Locate every Plasmodium falciparum-infected red blood cell.
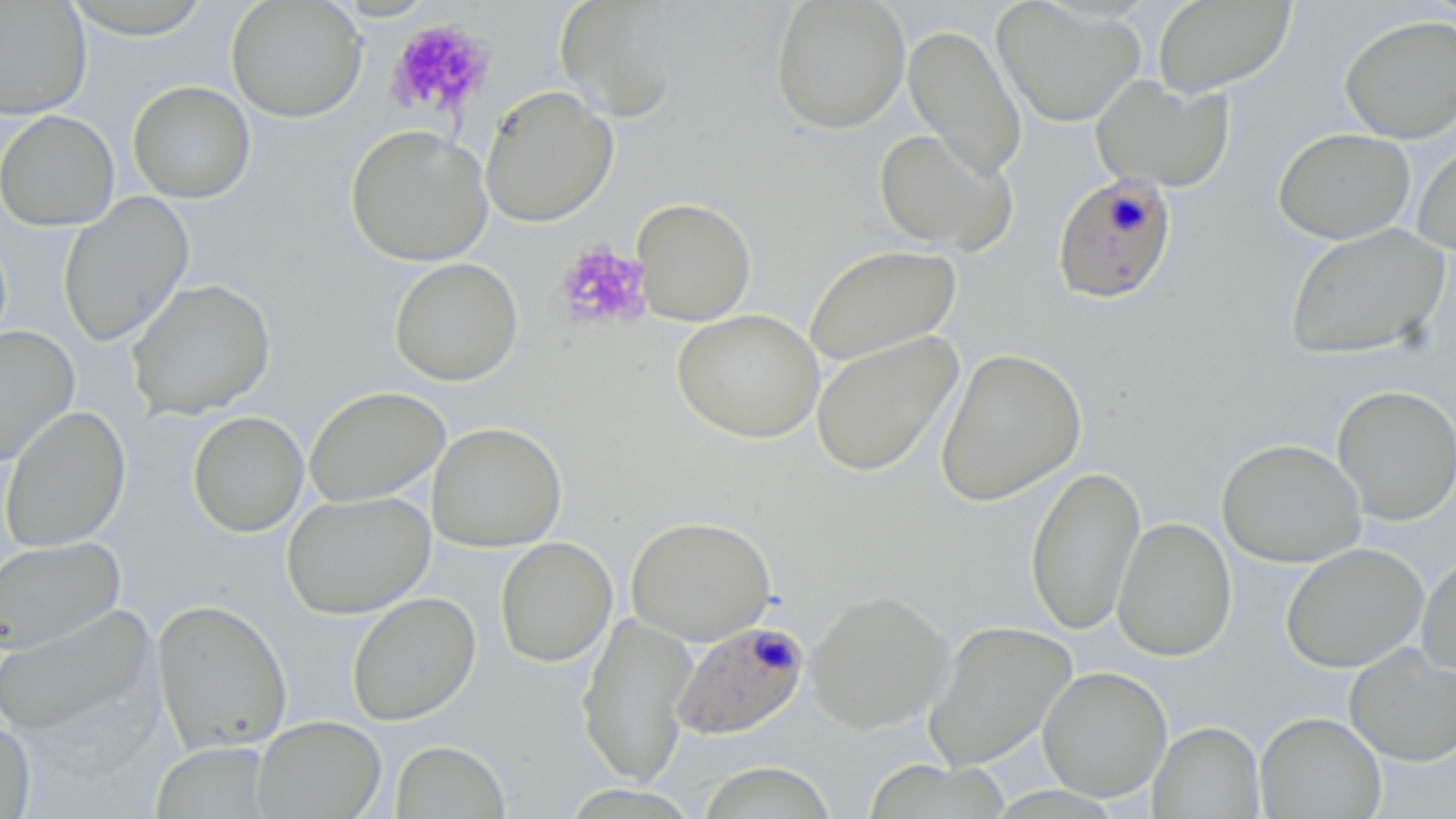

Approximate bounding boxes as [x1, y1, x2, y2] in pixels.
Plasmodium falciparum-infected red blood cells: [1051, 173, 1178, 306], [670, 620, 809, 740].

Platelet locations: [385, 19, 495, 119], [554, 241, 654, 333]. Uninfected red blood cell locations: [226, 0, 367, 123], [554, 0, 686, 122], [769, 0, 911, 135], [992, 0, 1146, 127], [1152, 0, 1295, 98], [0, 1, 92, 120], [61, 1, 217, 40], [1339, 14, 1456, 144], [903, 23, 1027, 183], [1090, 75, 1234, 193], [127, 80, 256, 203], [480, 84, 619, 228], [0, 110, 120, 231], [345, 124, 493, 267], [1273, 127, 1415, 244], [873, 128, 1017, 256], [1411, 136, 1456, 255], [57, 193, 195, 348], [631, 198, 757, 326], [1284, 223, 1452, 361], [802, 244, 962, 368], [389, 257, 523, 386], [126, 278, 276, 420], [672, 309, 824, 443], [0, 325, 79, 467], [810, 331, 963, 478], [934, 347, 1087, 507], [1331, 385, 1456, 525], [304, 386, 450, 507], [0, 404, 131, 553], [186, 411, 309, 538], [427, 422, 567, 551], [1216, 438, 1366, 568], [1025, 464, 1146, 636], [281, 491, 435, 619], [625, 515, 777, 645], [1112, 516, 1237, 661], [0, 536, 126, 655], [495, 537, 618, 667], [1280, 542, 1429, 673], [1416, 550, 1456, 680], [805, 588, 952, 733], [346, 592, 481, 726], [151, 598, 293, 754], [0, 604, 158, 739], [577, 611, 697, 788], [922, 620, 1078, 771], [1343, 643, 1456, 766], [1037, 666, 1173, 802], [1255, 711, 1386, 818], [252, 715, 387, 818], [0, 719, 36, 818], [1148, 721, 1265, 818], [389, 740, 511, 819], [150, 741, 275, 818], [861, 760, 1014, 818], [696, 761, 839, 819]. Slide-level diagnosis: Plasmodium falciparum. Image is 1456×819 pixels. 1000x magnification. Single field of view. Thin blood smear. Optical microscopy. May-Grünwald-Giemsa stain.